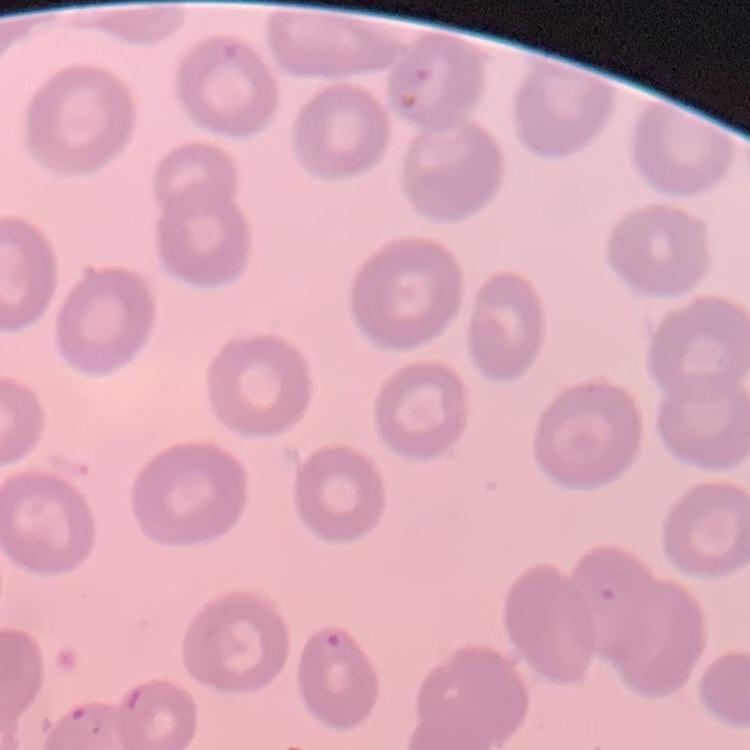
The red blood cells show no rouleaux formation. Thin blood smear. Square crop of a larger photomicrograph. Stained with either Field's or Giemsa.